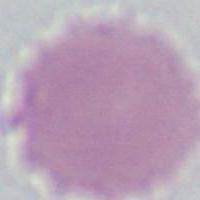
identification = erythrocyte
modality = photomicrograph
magnification = 1000x